Locate and identify every blood parasite.
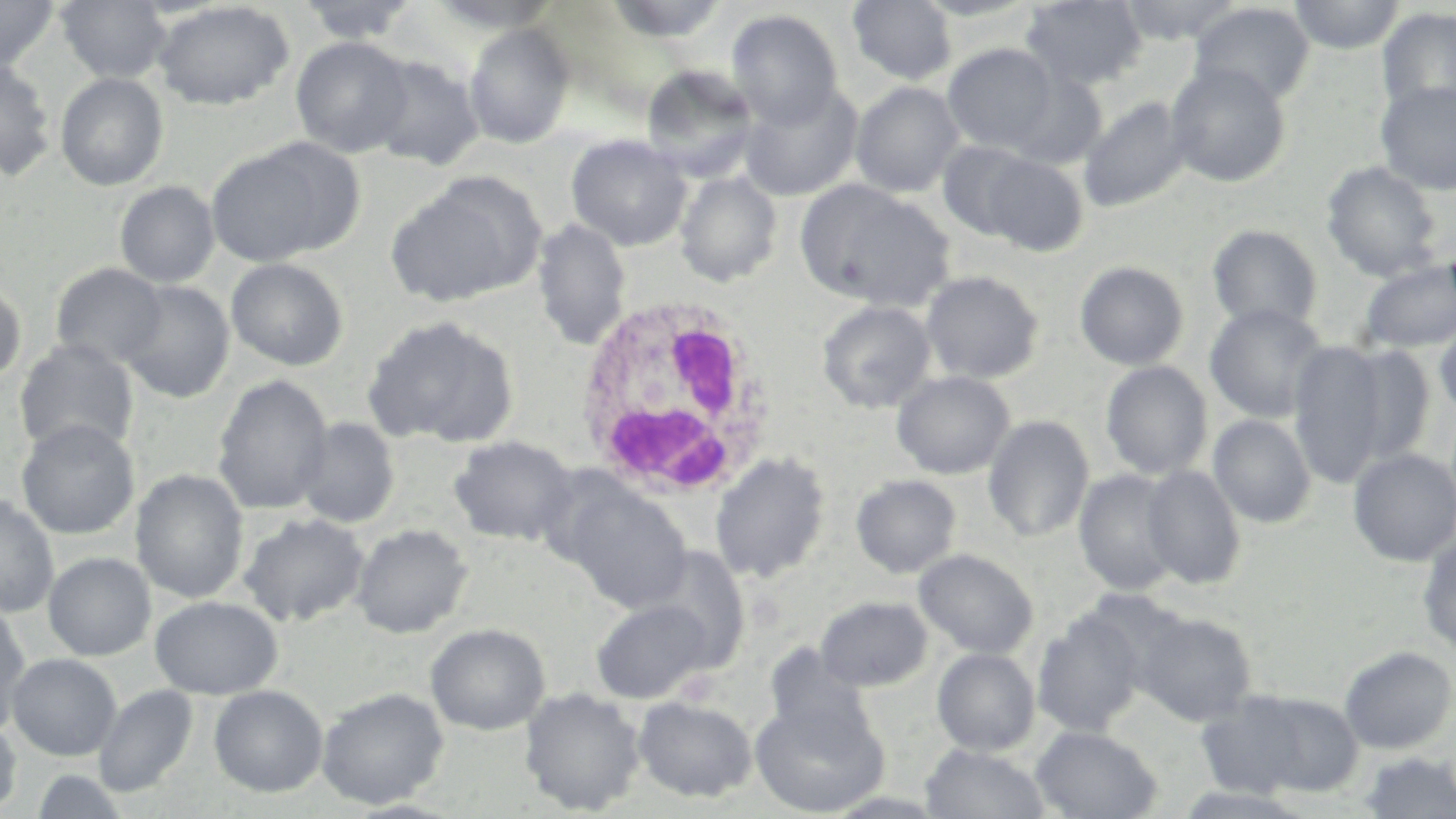
No blood parasites observed.

Summary:
  - Coordinate format: approximate bounding boxes as (x1,y1)-(x2,y2) corner pairs in pixels
  - Uninfected red blood cell locations: (0,0)-(61,73), (56,0)-(172,85), (296,0)-(422,45), (604,0)-(733,44), (848,0)-(957,87), (910,0)-(1042,23), (1020,0)-(1147,92), (1117,0)-(1247,45), (1288,0)-(1406,55), (427,1)-(565,34), (153,2)-(294,110), (1188,2)-(1315,110), (1376,6)-(1456,121), (726,9)-(844,131), (463,23)-(575,149), (291,36)-(414,159), (943,43)-(1062,156), (365,55)-(484,171), (0,58)-(57,182), (1165,61)-(1291,189), (640,63)-(760,184), (1002,70)-(1107,170), (55,72)-(169,191), (1374,79)-(1456,196), (738,80)-(863,202), (851,81)-(964,200), (1079,96)-(1191,214), (565,135)-(693,251), (936,140)-(1045,244), (206,145)-(343,267), (977,152)-(1089,257), (1321,161)-(1445,282), (676,171)-(782,289), (385,178)-(542,308), (794,178)-(954,312), (114,181)-(220,288), (531,218)-(631,351), (1206,224)-(1322,335), (226,258)-(349,371), (1356,258)-(1456,355), (1074,260)-(1190,371), (52,263)-(168,370), (919,270)-(1045,385), (0,278)-(26,390), (118,280)-(234,404), (817,300)-(937,414), (1204,302)-(1329,425), (362,315)-(520,449), (1433,316)-(1456,424), (14,338)-(139,459), (1289,338)-(1394,488), (1337,341)-(1435,474), (1100,360)-(1213,482), (891,370)-(1015,480), (213,375)-(334,515), (983,414)-(1094,544), (1208,414)-(1316,529), (294,417)-(400,529), (16,418)-(140,540), (448,435)-(578,546), (1348,447)-(1456,567), (710,451)-(831,584), (1140,464)-(1245,591), (131,469)-(249,605), (1074,469)-(1184,597), (851,475)-(961,578), (561,482)-(692,614), (0,493)-(59,618), (239,512)-(369,627), (352,523)-(472,639), (1417,531)-(1456,657), (636,547)-(751,675), (913,548)-(1038,659), (43,552)-(156,661), (149,595)-(283,699), (815,596)-(933,692), (591,598)-(715,704), (0,600)-(31,736), (1135,611)-(1257,727), (1033,612)-(1146,737), (426,623)-(549,736), (763,646)-(875,748), (1339,646)-(1456,755), (932,647)-(1040,757), (6,653)-(122,761), (94,685)-(198,799), (209,685)-(328,798), (317,687)-(449,810), (520,688)-(645,815), (1193,689)-(1342,801), (633,695)-(757,802), (749,696)-(888,816), (0,714)-(22,816), (1031,725)-(1161,819), (920,743)-(1052,819), (1356,751)-(1456,818), (30,768)-(132,819), (1170,785)-(1318,818)
  - White blood cell locations: (572,294)-(776,501)
  - Slide-level diagnosis: negative for blood parasites
  - Field of view: one of a larger specimen
  - Stain: May-Grünwald-Giemsa
  - Modality: optical microscopy
  - Magnification: 1000x
  - Image size: 1456×819 pixels
  - Preparation: thin blood film